Outline each blood parasite and name the species.
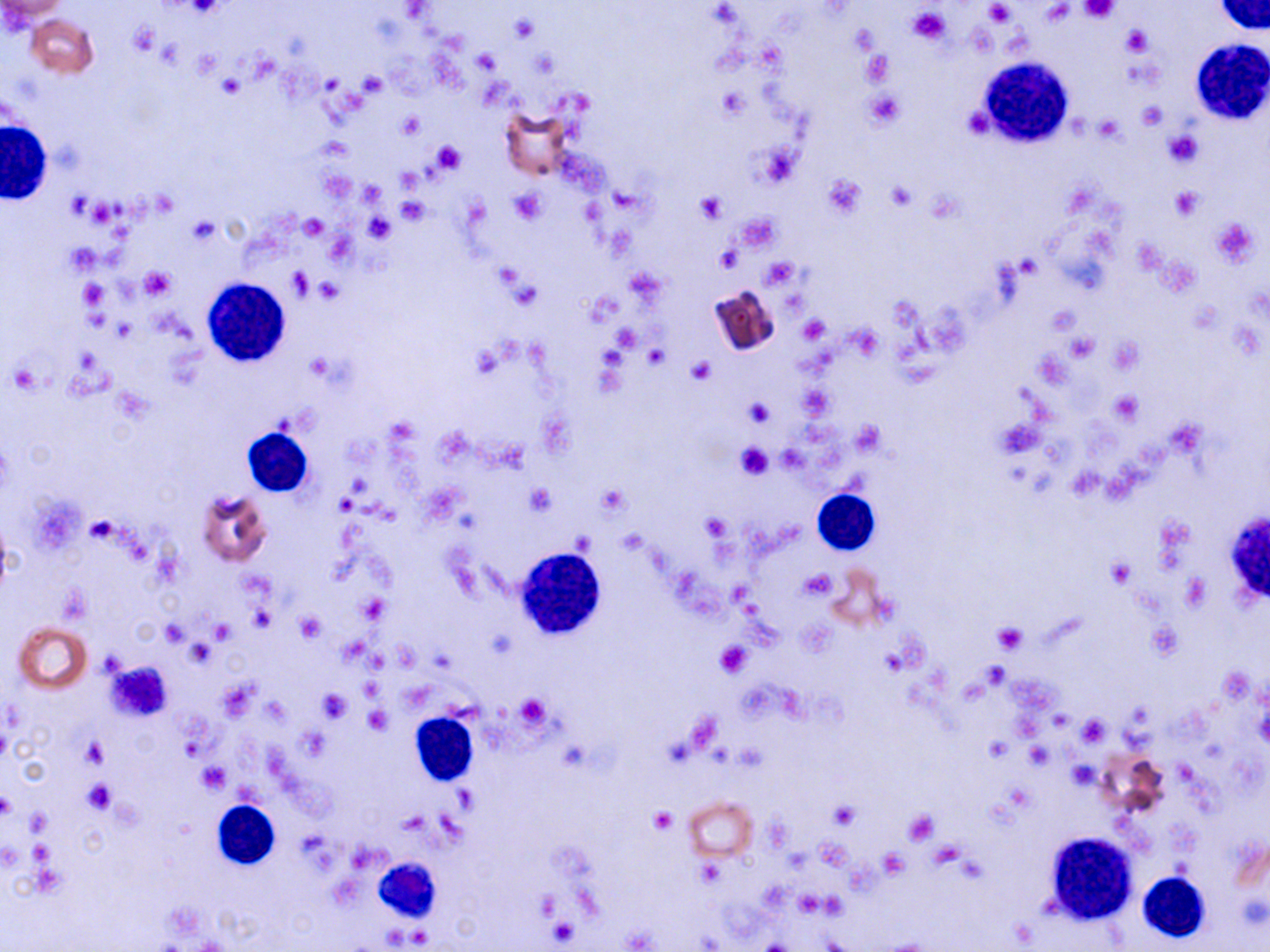
No blood parasites seen.

Summary:
  - Coordinate format: approximate bounding boxes as (x1,y1)-(x2,y2) corner pairs in pixels
  - Uninfected red blood cell locations (subset): (0,1)-(69,23), (25,13)-(99,78), (501,108)-(574,182), (708,284)-(782,358), (196,490)-(273,566), (830,566)-(890,630), (13,622)-(93,693), (1098,746)-(1170,820), (682,795)-(758,860)
  - Platelet locations: (181,1)-(226,18), (1081,1)-(1118,24), (984,3)-(1012,23), (1041,3)-(1075,26), (909,7)-(951,44), (129,22)-(160,57), (1123,26)-(1153,57), (473,50)-(500,75), (861,51)-(894,85), (358,72)-(387,96), (219,75)-(245,96), (865,89)-(904,129), (1136,102)-(1167,130), (963,107)-(993,138), (399,112)-(423,137), (1093,116)-(1124,142), (1165,131)-(1203,167), (433,140)-(462,173), (757,145)-(801,189), (823,175)-(866,217), (885,180)-(917,211), (358,182)-(385,207), (1171,187)-(1203,220), (511,189)-(544,225), (696,192)-(726,222), (396,197)-(428,223), (737,213)-(780,250), (365,214)-(395,241), (299,215)-(328,240), (187,216)-(219,245), (1211,217)-(1262,267), (64,241)-(101,275), (715,245)-(742,272), (761,257)-(800,287), (141,267)-(174,298), (287,267)-(313,298), (316,277)-(343,304), (78,280)-(109,310), (508,282)-(541,310), (800,316)-(828,342), (613,324)-(639,352), (1068,333)-(1097,362), (688,356)-(716,384), (9,365)-(39,392), (1110,392)-(1141,423), (744,398)-(774,428), (853,420)-(884,457), (735,443)-(774,479), (598,484)-(629,515), (525,485)-(555,514), (700,511)-(734,542), (85,516)-(117,543), (1109,559)-(1135,586), (801,569)-(834,599), (1182,575)-(1209,610), (59,587)-(92,625), (358,594)-(390,623), (248,608)-(275,632), (295,612)-(326,642), (209,619)-(235,642), (160,620)-(188,646), (992,621)-(1028,654), (186,642)-(215,667), (716,643)-(751,676), (106,661)-(173,719), (981,661)-(1010,688), (315,689)-(351,723), (515,694)-(549,729), (364,708)-(391,733), (1076,714)-(1110,747), (984,736)-(1011,761), (81,738)-(110,768), (1025,744)-(1051,769), (1067,760)-(1099,791), (199,763)-(228,793), (83,779)-(114,814), (0,793)-(18,820), (829,802)-(858,828), (650,807)-(675,833), (25,810)-(49,834), (903,810)-(938,844), (878,847)-(908,878), (696,860)-(724,887), (548,917)-(579,945)
  - White blood cell locations (subset): (1213,0)-(1268,36), (1190,39)-(1269,126), (978,60)-(1072,150), (1,122)-(51,204), (237,427)-(316,499), (813,488)-(879,556), (1227,508)-(1270,614), (514,547)-(605,640), (410,712)-(481,786), (212,800)-(280,871), (1044,831)-(1138,924), (378,857)-(448,928), (1138,872)-(1209,942)
  - Slide-level diagnosis: negative for blood parasites
  - Field of view: one of a larger specimen
  - Image size: 1270×952 pixels
  - Modality: light microscopy
  - Preparation: thin blood film
  - Stain: May-Grünwald-Giemsa
  - Magnification: 1000x